Give the extent of all Plasmodium ovale-infected red blood cells.
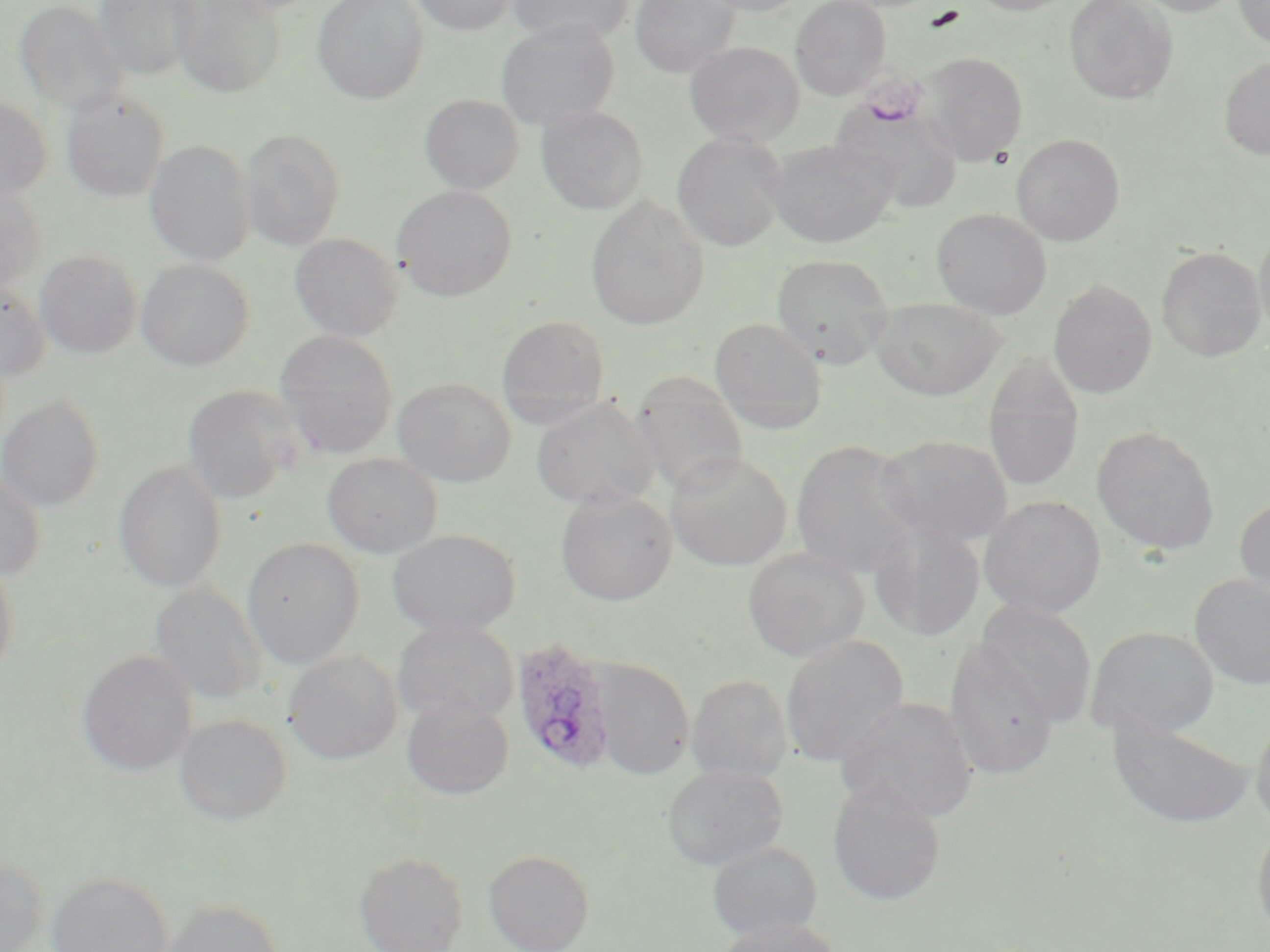

Approximate bounding boxes as named x1/y1/x2/y2 corners in pixels.
Plasmodium ovale-infected red blood cells: (x1=511, y1=637, x2=616, y2=777).

Summary:
  - Uninfected red blood cell locations: (x1=95, y1=0, x2=198, y2=79), (x1=170, y1=0, x2=287, y2=98), (x1=312, y1=0, x2=429, y2=104), (x1=409, y1=0, x2=516, y2=36), (x1=507, y1=0, x2=635, y2=45), (x1=629, y1=0, x2=739, y2=78), (x1=697, y1=0, x2=812, y2=16), (x1=789, y1=0, x2=891, y2=100), (x1=963, y1=0, x2=1082, y2=15), (x1=1064, y1=0, x2=1179, y2=105), (x1=1132, y1=0, x2=1244, y2=16), (x1=1233, y1=0, x2=1270, y2=50), (x1=14, y1=1, x2=127, y2=115), (x1=495, y1=19, x2=621, y2=129), (x1=684, y1=41, x2=805, y2=147), (x1=919, y1=52, x2=1028, y2=165), (x1=1219, y1=57, x2=1270, y2=161), (x1=60, y1=91, x2=169, y2=203), (x1=419, y1=94, x2=524, y2=195), (x1=0, y1=97, x2=52, y2=203), (x1=833, y1=105, x2=966, y2=216), (x1=535, y1=106, x2=648, y2=215), (x1=239, y1=128, x2=346, y2=251), (x1=1011, y1=133, x2=1126, y2=246), (x1=671, y1=134, x2=787, y2=251), (x1=764, y1=138, x2=899, y2=249), (x1=145, y1=140, x2=255, y2=266), (x1=0, y1=184, x2=47, y2=295), (x1=391, y1=186, x2=517, y2=301), (x1=585, y1=195, x2=710, y2=331), (x1=932, y1=208, x2=1052, y2=319), (x1=1253, y1=226, x2=1270, y2=348), (x1=289, y1=233, x2=405, y2=341), (x1=1156, y1=247, x2=1267, y2=361), (x1=34, y1=250, x2=143, y2=359), (x1=771, y1=253, x2=894, y2=369), (x1=136, y1=259, x2=254, y2=371), (x1=0, y1=279, x2=50, y2=382), (x1=1047, y1=280, x2=1158, y2=399), (x1=870, y1=297, x2=1007, y2=400), (x1=496, y1=315, x2=610, y2=422), (x1=709, y1=317, x2=827, y2=434), (x1=273, y1=331, x2=398, y2=458), (x1=983, y1=352, x2=1085, y2=493), (x1=630, y1=373, x2=749, y2=499), (x1=392, y1=378, x2=516, y2=486), (x1=181, y1=385, x2=302, y2=504), (x1=0, y1=395, x2=105, y2=513), (x1=530, y1=397, x2=659, y2=510), (x1=1092, y1=426, x2=1220, y2=556), (x1=876, y1=434, x2=1013, y2=548), (x1=790, y1=439, x2=922, y2=579), (x1=665, y1=450, x2=792, y2=571), (x1=322, y1=453, x2=442, y2=558), (x1=113, y1=462, x2=227, y2=593), (x1=0, y1=471, x2=46, y2=581), (x1=555, y1=489, x2=677, y2=606), (x1=979, y1=495, x2=1106, y2=618), (x1=1234, y1=496, x2=1270, y2=608), (x1=868, y1=521, x2=986, y2=642), (x1=386, y1=529, x2=521, y2=637), (x1=242, y1=537, x2=364, y2=669), (x1=743, y1=547, x2=869, y2=661), (x1=0, y1=556, x2=19, y2=683), (x1=1189, y1=573, x2=1270, y2=690), (x1=150, y1=579, x2=266, y2=705), (x1=974, y1=599, x2=1098, y2=728), (x1=392, y1=621, x2=518, y2=725), (x1=1085, y1=626, x2=1220, y2=739), (x1=780, y1=634, x2=909, y2=767), (x1=944, y1=637, x2=1059, y2=781), (x1=77, y1=650, x2=197, y2=777), (x1=284, y1=650, x2=402, y2=765), (x1=591, y1=658, x2=694, y2=780), (x1=686, y1=675, x2=793, y2=781), (x1=400, y1=693, x2=515, y2=799), (x1=836, y1=697, x2=978, y2=823), (x1=1250, y1=709, x2=1270, y2=831), (x1=174, y1=713, x2=291, y2=825), (x1=1106, y1=715, x2=1256, y2=830), (x1=662, y1=764, x2=788, y2=870), (x1=827, y1=780, x2=947, y2=907), (x1=1252, y1=819, x2=1270, y2=943), (x1=708, y1=841, x2=822, y2=941), (x1=483, y1=849, x2=595, y2=952), (x1=353, y1=851, x2=469, y2=952), (x1=0, y1=856, x2=49, y2=952), (x1=46, y1=871, x2=174, y2=952), (x1=159, y1=898, x2=284, y2=952), (x1=715, y1=919, x2=842, y2=952)
  - Platelet locations: (x1=922, y1=6, x2=965, y2=32)
  - Slide-level diagnosis: Plasmodium ovale
  - Field of view: one of a larger specimen
  - Magnification: 1000x
  - Stain: May-Grünwald-Giemsa
  - Modality: light microscopy
  - Preparation: thin blood smear
  - Image size: 1270×952 pixels